Locate leukocytes (white blood cells).
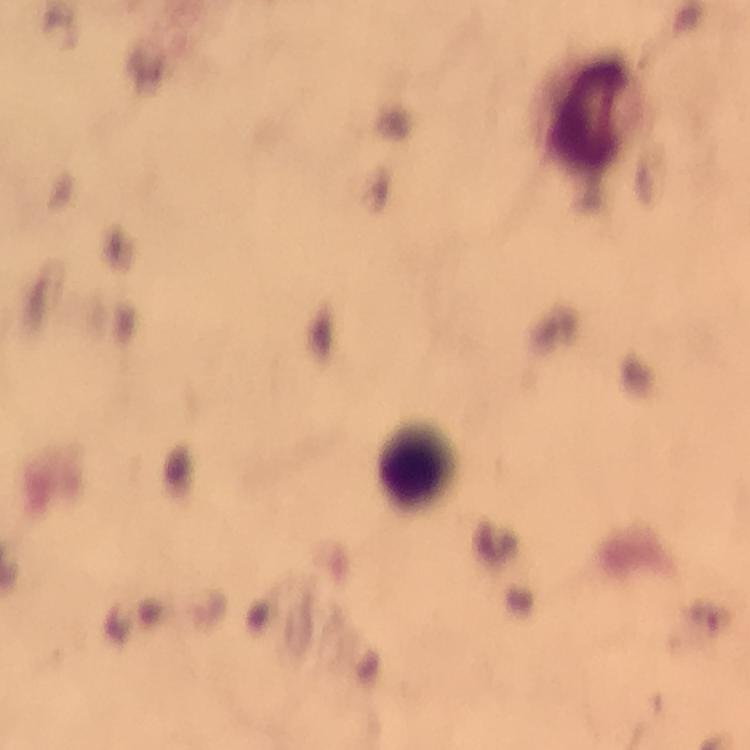

Approximate object centers, in pixels from the top-left corner.
Leukocytes: (x=581, y=114), (x=418, y=466).

Summary:
  - Image size: 750×750 pixels
  - Capture: smartphone camera through the microscope
  - Magnification: 100x
  - Immersion oil: used
  - Stain: Giemsa
  - Cropped from: a single field of view
  - Context: from a diagnostic examination for malaria
  - Plasmodium parasites: none seen
  - Preparation: thick smear